Locate every blood parasite and identify its species.
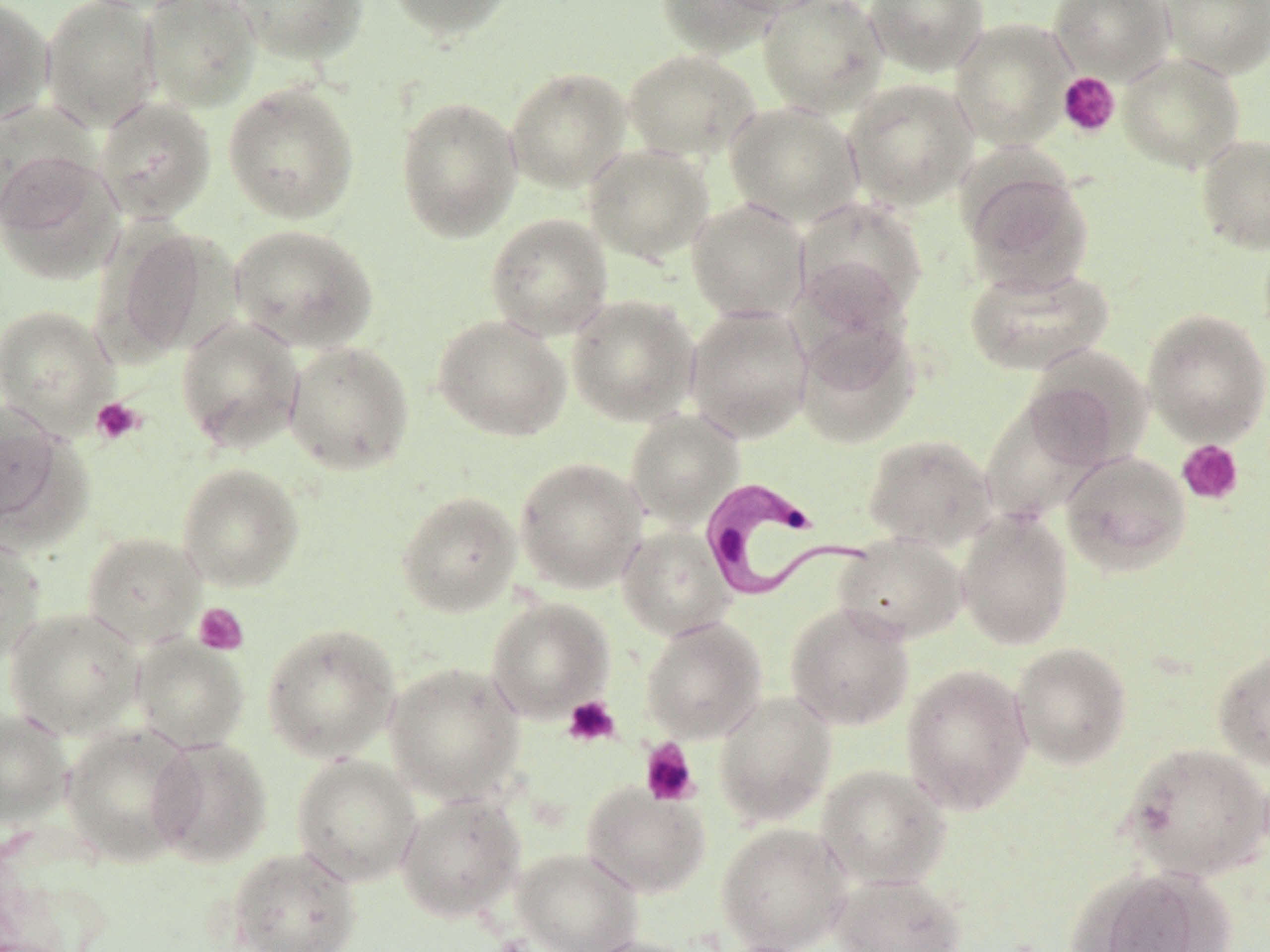
Approximate bounding boxes as [x1, y1, x2, y2] in pixels.
Trypanosoma brucei: [699, 476, 874, 604].
No Plasmodium falciparum, Plasmodium ovale, Plasmodium malariae, Plasmodium vivax, or Babesia divergens observed.

slide-level diagnosis = Trypanosoma brucei
stain = May-Grünwald-Giemsa
uninfected red blood cell locations (subset) = approximate bounding boxes as [x1, y1, x2, y2] in pixels: [0, 0, 54, 124], [40, 0, 162, 131], [140, 0, 261, 112], [230, 0, 369, 65], [385, 0, 516, 40], [655, 0, 781, 57], [715, 0, 835, 17], [757, 0, 887, 117], [864, 0, 989, 76], [1050, 0, 1175, 83], [1161, 0, 1270, 78], [622, 49, 761, 163], [1117, 52, 1246, 174], [505, 66, 631, 192], [843, 78, 979, 211], [223, 81, 360, 224], [395, 95, 523, 242], [94, 97, 216, 224], [1, 101, 97, 228], [725, 101, 865, 228], [1195, 133, 1270, 254], [583, 143, 714, 263], [0, 150, 125, 286], [962, 165, 1095, 294], [793, 196, 928, 327], [686, 198, 811, 322], [485, 213, 614, 340], [230, 223, 379, 353], [103, 224, 218, 361], [964, 264, 1114, 376], [566, 294, 700, 427], [0, 304, 120, 436], [684, 305, 814, 443], [1142, 308, 1270, 445], [433, 314, 572, 441], [176, 316, 303, 453], [793, 320, 921, 449], [283, 340, 415, 475], [1020, 350, 1149, 472], [980, 396, 1106, 523], [1, 403, 69, 536], [625, 409, 744, 528], [863, 433, 997, 551], [1060, 450, 1191, 576], [515, 457, 648, 593], [176, 463, 305, 591], [396, 490, 522, 617], [956, 507, 1074, 649], [617, 525, 735, 640], [82, 531, 206, 648], [833, 532, 967, 645], [0, 535, 46, 665], [486, 597, 615, 722], [785, 602, 915, 730], [4, 607, 144, 739], [640, 617, 767, 743], [262, 623, 401, 762], [130, 635, 250, 753], [1010, 642, 1132, 769], [1212, 649, 1270, 771], [384, 661, 525, 804], [900, 664, 1034, 815], [713, 691, 837, 826], [0, 708, 73, 827], [61, 723, 197, 865], [148, 736, 272, 868], [1120, 742, 1270, 882], [291, 754, 422, 886], [816, 764, 951, 890], [581, 781, 710, 898], [395, 792, 525, 923], [716, 823, 852, 952], [227, 846, 361, 952], [512, 847, 643, 952], [1068, 866, 1224, 952], [831, 872, 967, 952], [581, 936, 701, 952]
modality = light microscopy
magnification = 1000x
platelet locations (subset) = approximate bounding boxes as [x1, y1, x2, y2] in pixels: [1057, 72, 1120, 138], [91, 397, 145, 444], [1176, 439, 1244, 506], [193, 602, 248, 655], [562, 696, 620, 747], [640, 739, 700, 807]
image size = 1270×952 pixels
preparation = thin blood film
field of view = single